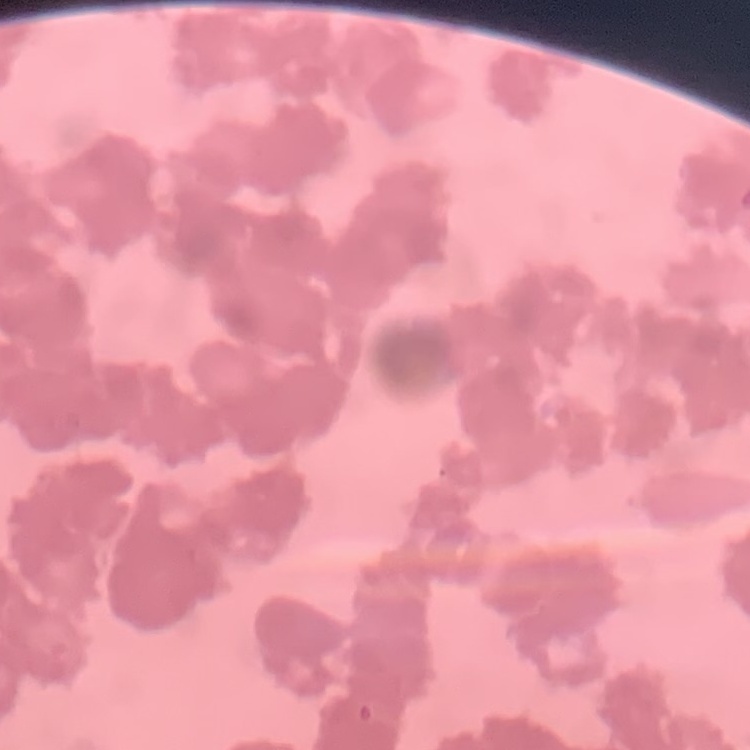
Summary:
  - Red blood cell morphology: rouleaux formation
  - Stain: Field's or Giemsa
  - Image type: square crop of a larger photomicrograph
  - Preparation: thin blood smear